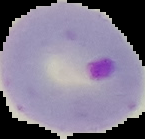
Summary:
  - Preparation: thin blood film
  - Result: Plasmodium parasites detected
  - Image type: segmented cell region with the area outside set to black
  - Image size: 145×139 pixels